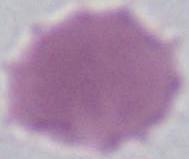
Captured at 1000x magnification. Micrograph. A red blood cell is seen.